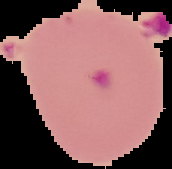

image type = segmented cell region on a black background
image size = 172×169 pixels
preparation = thin blood smear
malaria status = parasitized